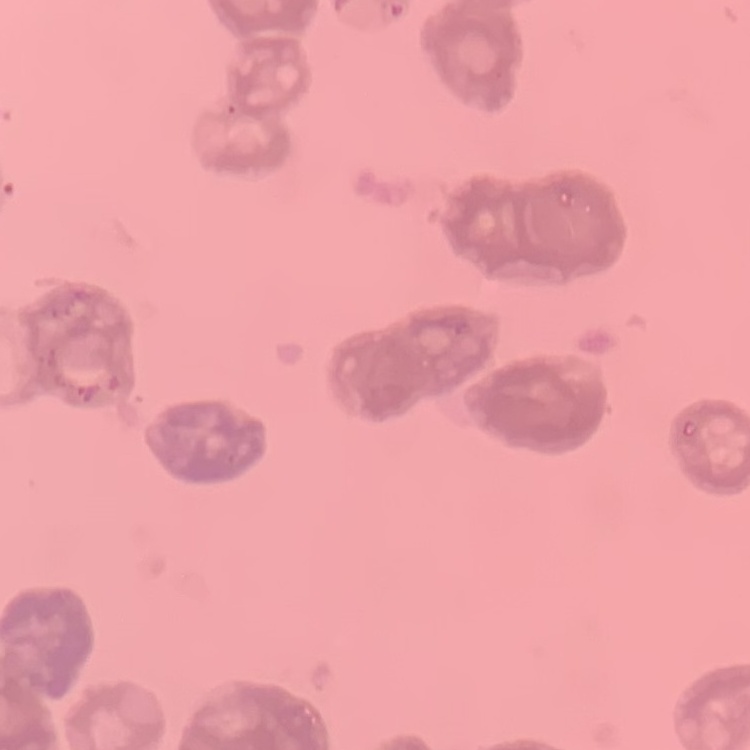

Summary:
  - Erythrocyte morphology: rouleaux formation
  - Stain: Field's or Giemsa
  - Image type: one tile cut from a larger photomicrograph
  - Preparation: thin peripheral smear